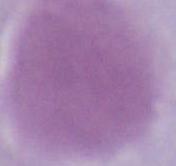

magnification = 1000x
modality = micrograph
identification = erythrocyte